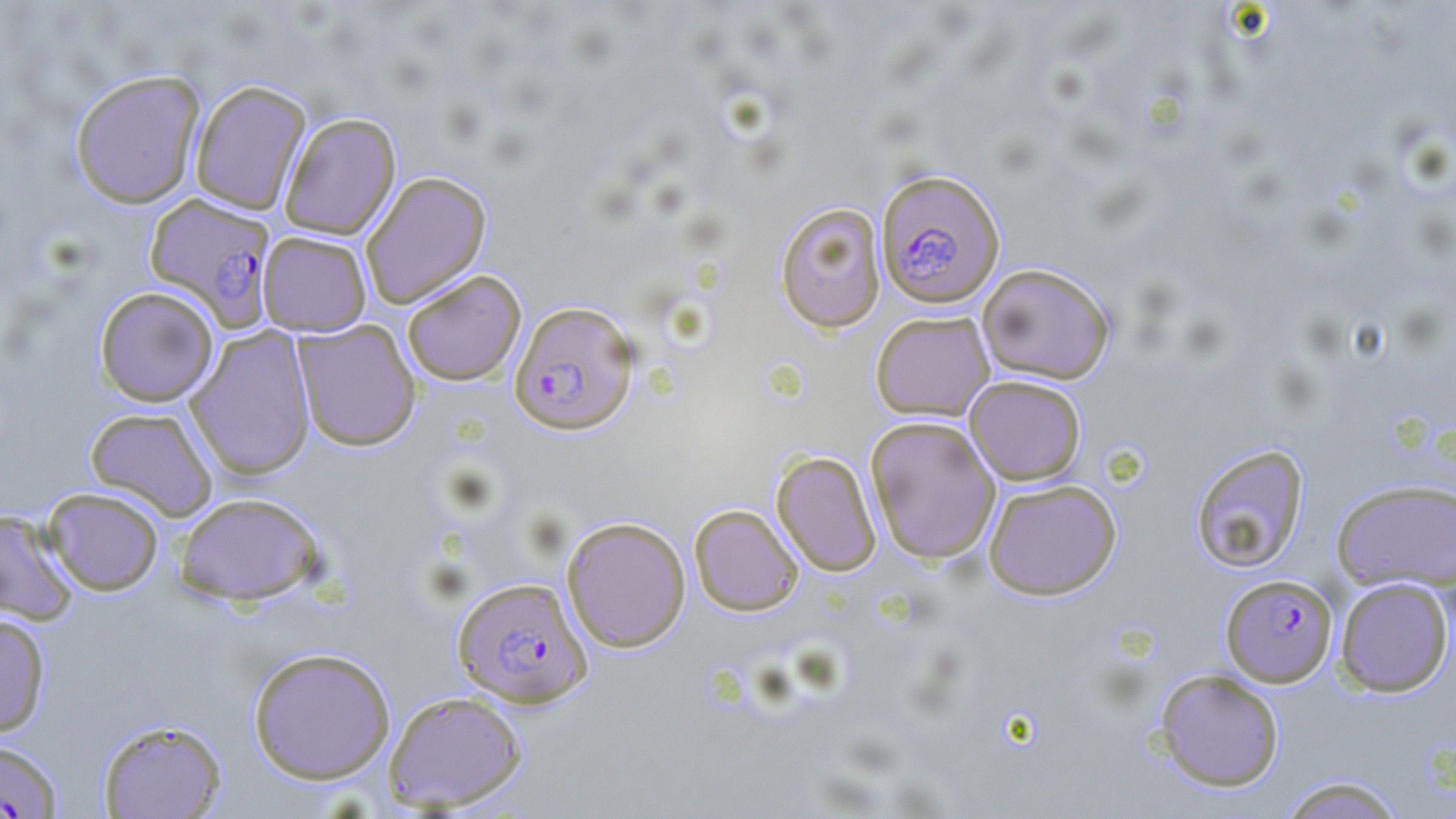
Approximate bounding boxes as (x1,y1)-(x2,y2) corner pairs in pixels. Plasmodium falciparum-infected red blood cell locations: (875,169)-(1006,308), (144,192)-(276,329), (509,301)-(639,435), (1221,573)-(1338,687), (452,576)-(593,708), (0,738)-(64,818). Uninfected red blood cell locations: (70,69)-(205,209), (189,79)-(313,215), (278,112)-(401,239), (360,170)-(492,309), (774,201)-(887,333), (258,231)-(371,336), (977,263)-(1115,384), (402,269)-(526,386), (94,286)-(219,407), (870,310)-(995,421), (293,320)-(421,451), (186,325)-(317,480), (964,375)-(1087,485), (85,406)-(219,521), (865,416)-(1001,564), (1189,443)-(1310,574), (771,450)-(882,576), (1330,477)-(1456,594), (983,479)-(1121,599), (42,487)-(164,596), (174,492)-(326,605), (689,504)-(803,616), (0,508)-(80,625), (561,516)-(691,653), (1335,577)-(1454,697), (0,613)-(51,737), (247,647)-(396,784), (1154,669)-(1285,792), (383,690)-(528,812), (95,717)-(228,818), (1278,774)-(1407,819). Slide-level diagnosis: Plasmodium falciparum. Light microscopy. 1000x magnification. Thin blood smear. One field of a larger specimen. May-Grünwald-Giemsa stain. Image is 1456×819 pixels.